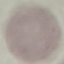

malaria status = uninfected
stain = Giemsa
image type = automatically extracted cell patch, resized to 64 × 64 pixels
capture = smartphone through the microscope eyepiece
preparation = thin smear